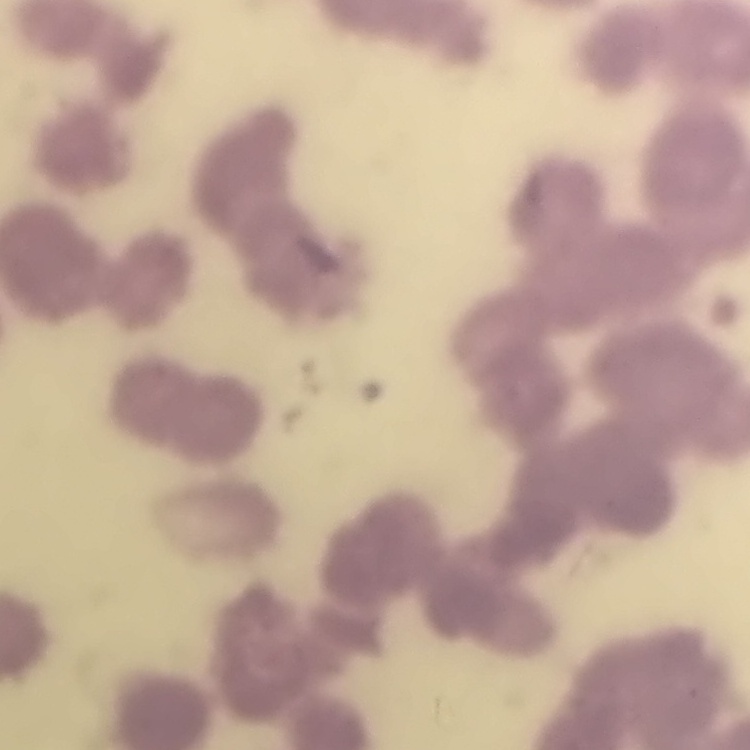 The erythrocytes exhibit rouleaux formation. Field's or Giemsa stain. Thin blood film. One tile cut from a larger photomicrograph.